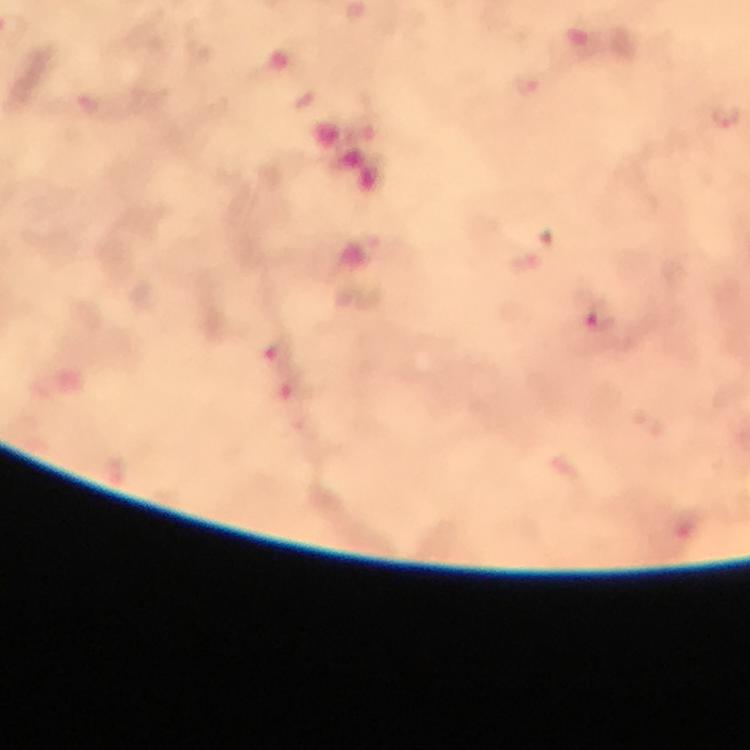

Approximate centers as [x, y] in pixels. Plasmodium parasite locations: [726, 119], [600, 323], [278, 355]. Image is 750×750 pixels. Thick smear. Giemsa stain. Immersion oil applied. At 100x magnification. A crop from one field of view. Smartphone photograph taken through a microscope. From a diagnostic examination for malaria.